Identify the parasite.
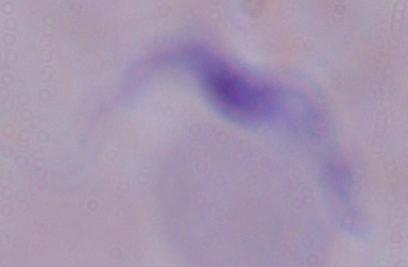
This is a trypanosome.

1000x magnification. Micrograph.